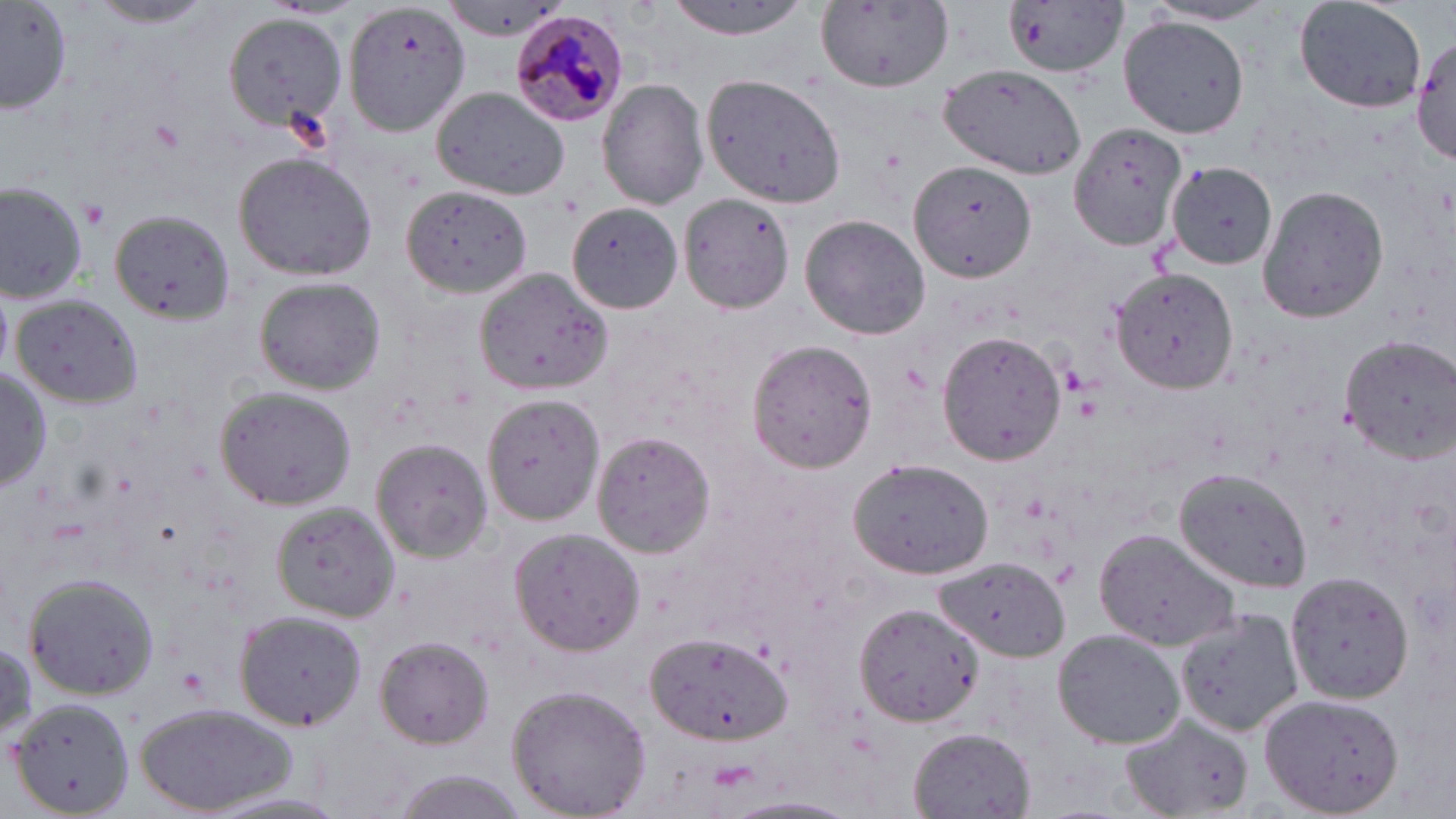

Summary:
  - Coordinate format: approximate bounding boxes as (x1,y1)-(x2,y2) corner pairs in pixels
  - Uninfected red blood cell locations: (665,0)-(813,41), (343,1)-(472,138), (811,1)-(954,96), (1001,1)-(1131,80), (1291,1)-(1426,113), (86,2)-(221,28), (1146,2)-(1282,26), (1,4)-(74,115), (441,5)-(566,42), (221,10)-(350,137), (1119,14)-(1250,137), (1411,32)-(1456,163), (939,63)-(1087,180), (701,73)-(845,207), (598,77)-(710,211), (430,86)-(570,199), (1069,122)-(1189,255), (233,153)-(377,282), (910,160)-(1035,284), (1165,165)-(1278,272), (0,179)-(90,305), (401,185)-(533,297), (1255,185)-(1390,324), (678,194)-(799,314), (568,202)-(684,318), (801,213)-(932,341), (110,214)-(236,325), (1110,267)-(1238,394), (476,269)-(613,398), (254,278)-(386,393), (12,295)-(143,409), (937,327)-(1068,468), (1338,333)-(1456,464), (747,338)-(879,472), (2,366)-(51,493), (213,387)-(357,510), (483,393)-(605,522), (592,430)-(715,557), (370,437)-(493,562), (847,457)-(995,579), (1173,466)-(1315,590), (271,503)-(402,623), (1093,526)-(1241,649), (508,527)-(644,655), (936,557)-(1070,658), (1284,572)-(1414,704), (23,574)-(159,701), (853,603)-(983,726), (1177,608)-(1305,740), (234,610)-(367,731), (1052,628)-(1185,749), (647,632)-(792,749), (375,636)-(494,748), (504,683)-(653,819), (1261,690)-(1405,819), (8,697)-(134,819), (135,702)-(300,817), (1120,714)-(1253,818), (909,728)-(1036,818), (378,769)-(538,818), (721,795)-(861,817)
  - Platelet locations: (79,200)-(111,228), (1049,562)-(1080,588)
  - Plasmodium malariae-infected red blood cell locations: (508,10)-(631,128)
  - Slide-level diagnosis: Plasmodium malariae
  - Stain: May-Grünwald-Giemsa
  - Modality: optical microscopy
  - Magnification: 1000x
  - Field of view: single
  - Preparation: thin blood smear
  - Image size: 1456×819 pixels